Assess for malaria.
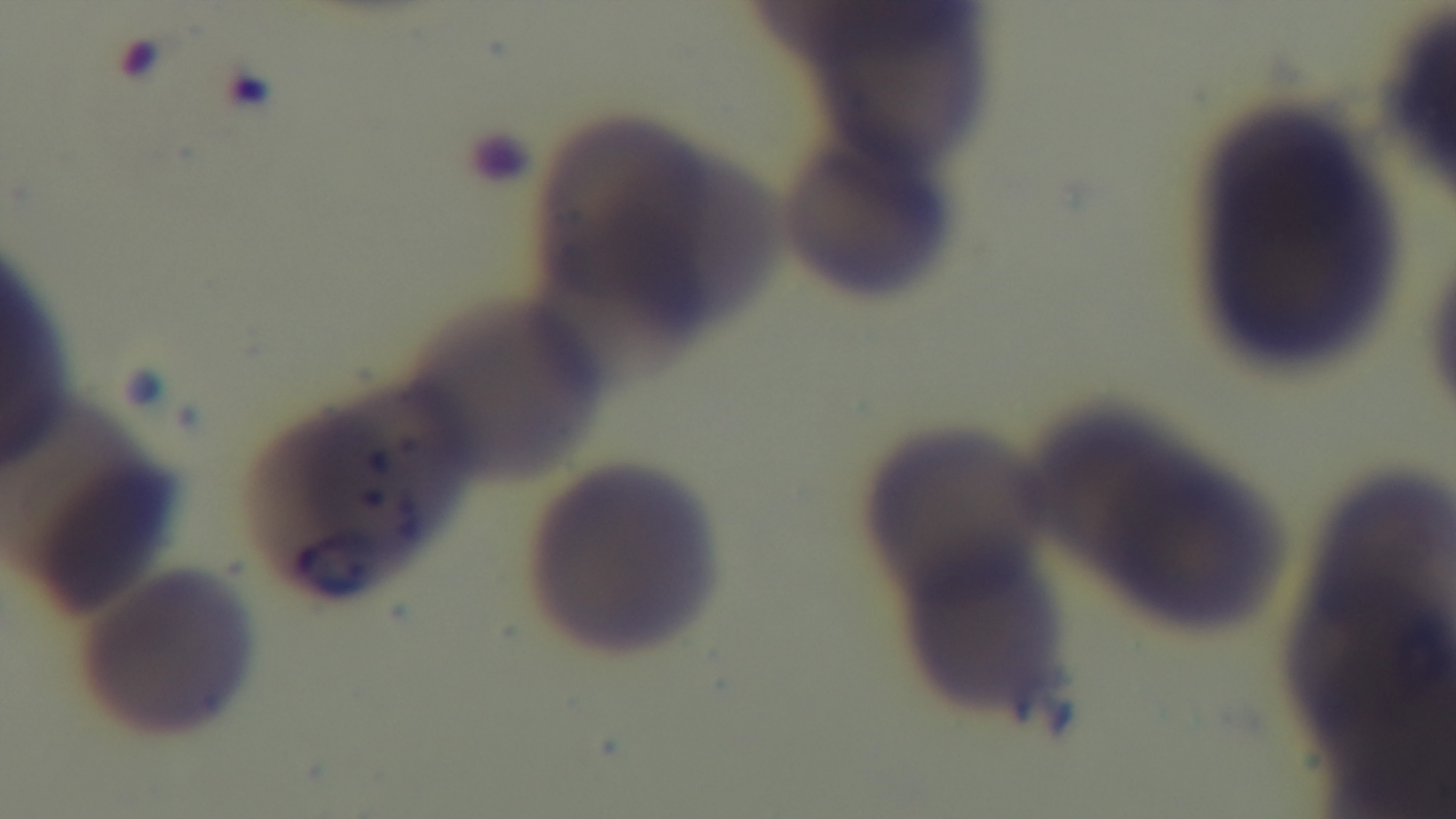

Infected.

Giemsa stain. One field from the slide. Oil-immersion objective, 100x. Photomicrograph. Mounted 4K digital camera. Preparation: thin.